Give the extent of all Plasmodium malariae-infected red blood cells.
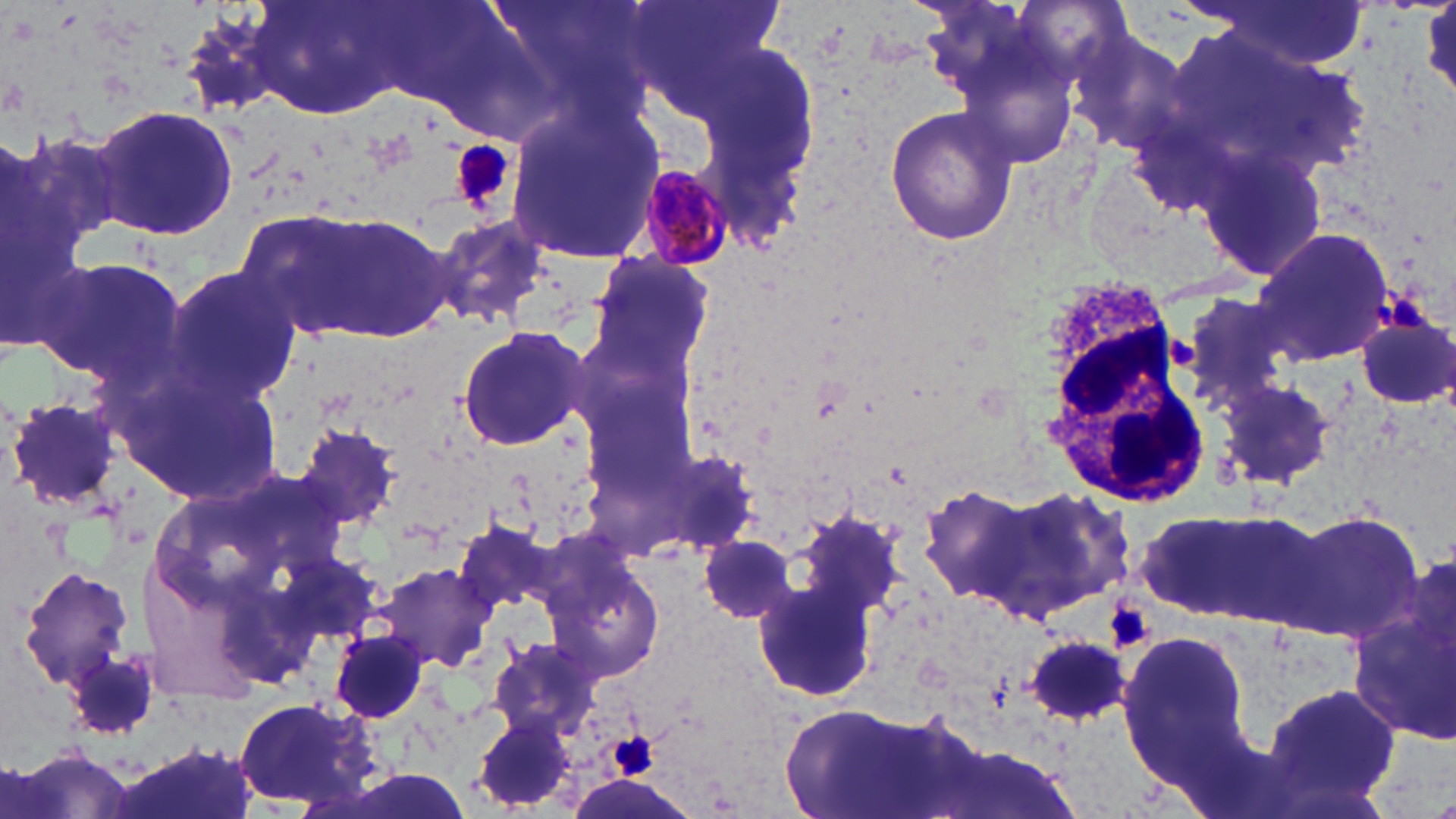
Approximate bounding boxes as [x1, y1, x2, y2] in pixels.
Plasmodium malariae-infected red blood cells: [631, 160, 736, 271].

Summary:
  - Platelet locations: [454, 141, 514, 209], [1378, 286, 1424, 329], [1107, 600, 1156, 651], [612, 731, 658, 778]
  - White blood cell locations: [1037, 274, 1203, 503]
  - Uninfected red blood cell locations: [488, 0, 654, 115], [627, 0, 788, 122], [246, 1, 423, 125], [1190, 2, 1372, 73], [1063, 24, 1196, 160], [507, 100, 666, 269], [91, 103, 239, 243], [885, 103, 1021, 247], [1183, 103, 1341, 278], [2, 115, 110, 367], [253, 206, 454, 345], [426, 215, 554, 331], [1249, 226, 1396, 364], [585, 252, 716, 385], [36, 254, 187, 391], [162, 263, 301, 407], [1178, 292, 1297, 412], [1354, 310, 1456, 409], [455, 324, 593, 452], [1214, 377, 1335, 488], [6, 396, 123, 513], [292, 421, 397, 533], [652, 446, 759, 559], [916, 483, 1051, 609], [991, 487, 1137, 624], [1137, 507, 1324, 628], [1286, 509, 1427, 646], [453, 518, 558, 625], [702, 533, 795, 622], [548, 558, 666, 685], [376, 561, 496, 671], [16, 567, 136, 694], [754, 574, 882, 702], [1351, 585, 1456, 748], [1117, 627, 1253, 774], [331, 629, 431, 722], [1025, 633, 1137, 726], [488, 636, 602, 742], [64, 641, 165, 746], [1260, 679, 1403, 813], [228, 698, 382, 810], [779, 699, 943, 819], [474, 711, 577, 812]
  - Slide-level diagnosis: Plasmodium malariae
  - Preparation: thin blood smear
  - Field of view: one of a larger specimen
  - Stain: May-Grünwald-Giemsa
  - Modality: optical microscopy
  - Image size: 1456×819 pixels
  - Magnification: 1000x